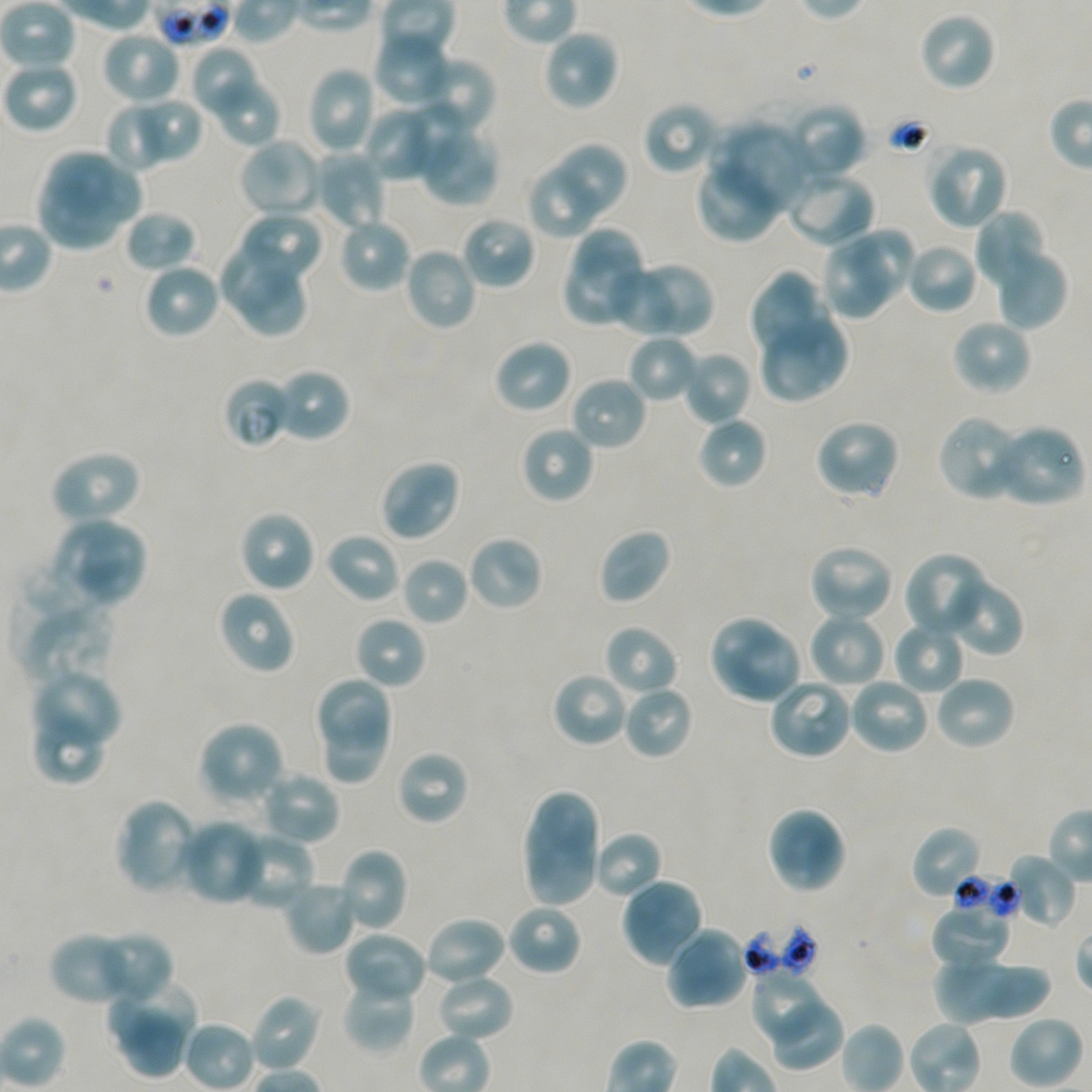
Approximate bounding boxes as {x1, y1, x2, y2} in pixels. Not every red blood cell is marked. Locations of uninfected red blood cells: {0, 0, 73, 70}, {917, 11, 997, 92}, {541, 28, 619, 112}, {101, 29, 182, 105}, {373, 35, 447, 109}, {188, 45, 262, 121}, {2, 60, 80, 134}, {421, 60, 495, 136}, {306, 66, 378, 155}, {211, 73, 283, 147}, {109, 97, 200, 172}, {141, 99, 202, 160}, {403, 99, 469, 184}, {109, 101, 164, 172}, {642, 101, 720, 176}, {786, 102, 867, 182}, {363, 105, 443, 183}, {712, 121, 810, 218}, {417, 124, 500, 208}, {238, 137, 324, 220}, {926, 142, 1008, 231}, {558, 143, 629, 215}, {43, 145, 147, 225}, {312, 150, 386, 232}, {695, 156, 781, 243}, {527, 165, 597, 240}, {31, 166, 134, 259}, {784, 169, 875, 249}, {973, 208, 1049, 295}, {124, 209, 198, 274}, {238, 211, 325, 285}, {459, 214, 536, 291}, {336, 217, 412, 293}, {574, 220, 648, 299}, {848, 225, 916, 306}, {821, 240, 890, 321}, {905, 240, 979, 315}, {218, 244, 295, 318}, {992, 246, 1068, 331}, {403, 247, 479, 333}, {562, 253, 638, 329}, {631, 261, 714, 338}, {142, 262, 221, 340}, {605, 265, 680, 336}, {236, 270, 308, 335}, {749, 271, 828, 362}, {758, 313, 848, 403}, {950, 317, 1032, 396}, {627, 335, 700, 405}, {492, 338, 574, 416}, {681, 350, 752, 426}, {274, 367, 352, 443}, {568, 376, 649, 453}, {936, 413, 1025, 502}, {697, 416, 768, 490}, {813, 418, 900, 501}, {519, 424, 595, 505}, {990, 424, 1085, 509}, {49, 448, 142, 525}, {378, 458, 462, 542}, {48, 509, 124, 598}, {238, 509, 316, 593}, {78, 523, 147, 608}, {598, 527, 672, 605}, {325, 532, 401, 604}, {467, 534, 543, 612}, {807, 543, 895, 623}, {903, 551, 991, 640}, {400, 556, 469, 626}, {940, 573, 1024, 657}, {217, 589, 297, 675}, {18, 600, 114, 691}, {807, 611, 888, 689}, {707, 613, 782, 693}, {353, 615, 426, 690}, {892, 619, 966, 695}, {602, 623, 680, 697}, {726, 631, 803, 706}, {32, 671, 122, 752}, {312, 671, 395, 750}, {550, 671, 630, 748}, {932, 674, 1017, 752}, {767, 676, 854, 761}, {848, 676, 930, 755}, {621, 685, 695, 761}, {322, 704, 390, 790}, {31, 706, 107, 785}, {198, 721, 286, 807}, {395, 749, 471, 826}, {259, 769, 341, 847}, {522, 788, 601, 909}, {115, 797, 202, 895}, {765, 806, 846, 895}, {180, 819, 266, 905}, {910, 825, 984, 900}, {592, 830, 663, 901}, {229, 831, 315, 912}, {338, 846, 408, 933}, {1006, 852, 1076, 930}, {620, 877, 705, 968}, {284, 879, 360, 955}, {506, 903, 583, 976}, {931, 905, 1012, 970}, {423, 915, 507, 988}, {664, 926, 750, 1011}, {95, 930, 173, 1004}, {344, 930, 428, 1004}, {48, 931, 135, 1006}, {933, 958, 1052, 1025}, {933, 960, 1015, 1025}, {983, 962, 1052, 1023}, {434, 970, 515, 1042}, {749, 970, 830, 1047}, {341, 973, 417, 1053}, {107, 979, 202, 1049}, {249, 992, 323, 1073}, {767, 998, 845, 1074}, {117, 1006, 192, 1082}, {1008, 1015, 1083, 1089}. Locations of red blood cells of indeterminate infection status: {223, 376, 295, 448}, {950, 872, 1019, 922}. Giemsa stain. 100x oil-immersion objective, numerical aperture 1.45. One field from this slide. Thin blood film. Plasmodium falciparum strain NF54 maintained in static in-vitro culture. Image is 1092×1092 pixels. Donor blood group A+/O+.